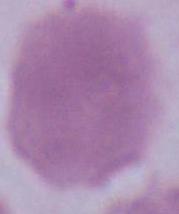

identification = erythrocyte
modality = micrograph
magnification = 1000x